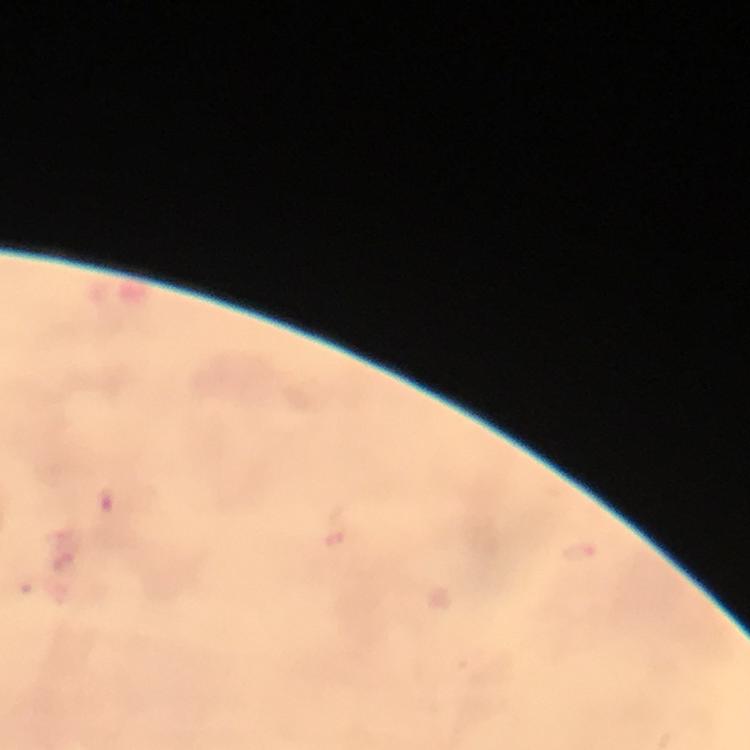
Approximate centers as {x, y} in pixels. Malaria parasite locations: {106, 502}, {335, 537}, {63, 549}, {583, 552}. Image is 750×750 pixels. Immersion oil was used. Photographed with a smartphone mounted on the microscope. Giemsa stain. From a malaria diagnostic workup. Cropped region of a single field of view. 100x magnification. Thick blood film.